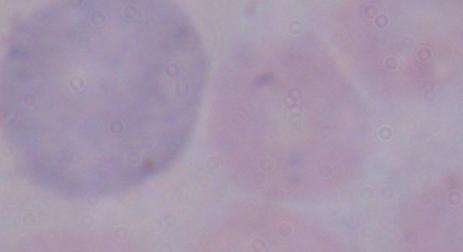
Summary:
  - Modality: micrograph
  - Identification: trypanosome
  - Magnification: 1000x